Give the extent of all Trypanosoma brucei.
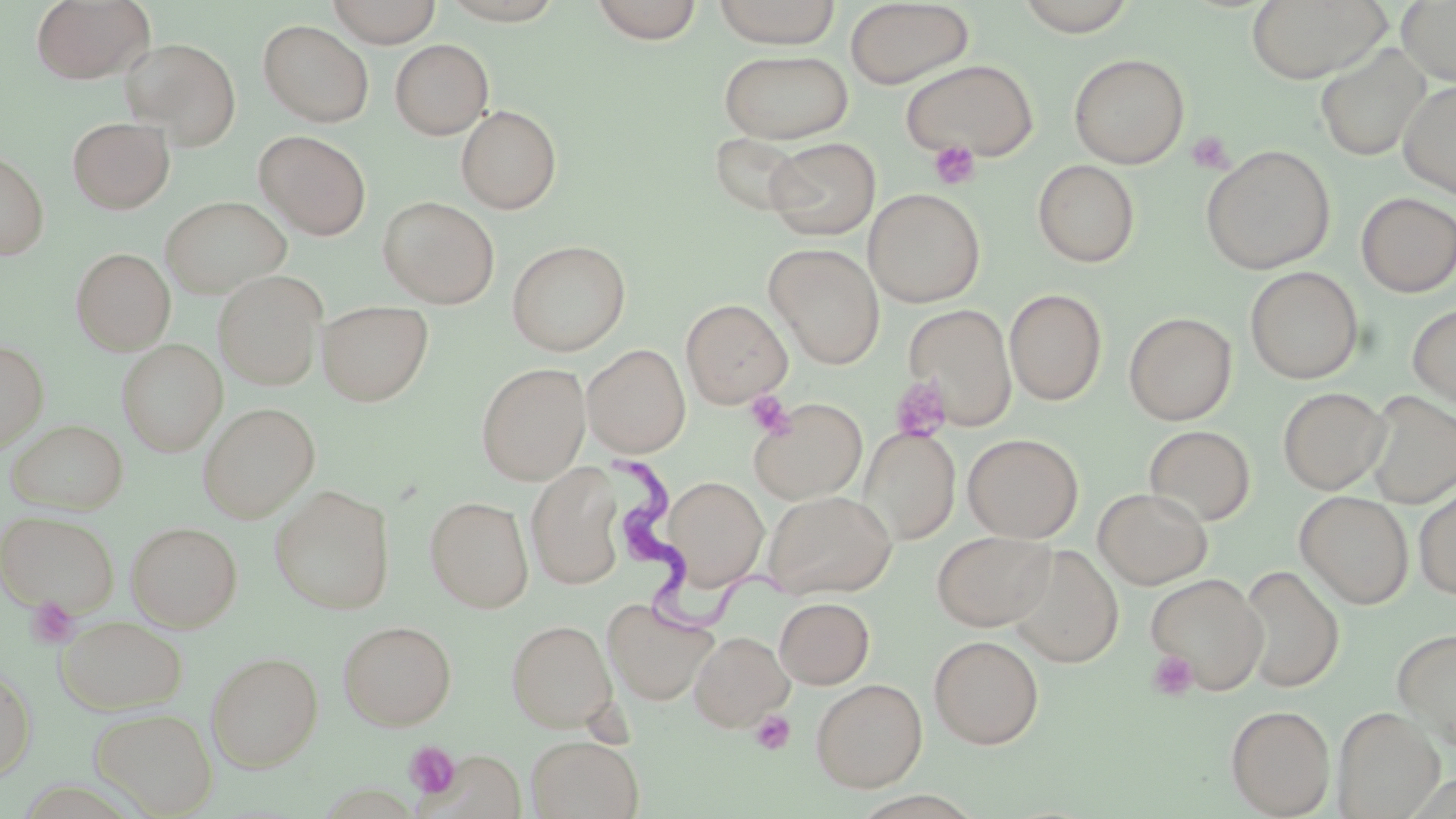

Approximate bounding boxes as [x1, y1, x2, y2] in pixels.
Trypanosoma brucei: [614, 454, 787, 636].

slide_level_diagnosis: Trypanosoma brucei
preparation: thin blood film
platelet_locations: 'approximate bounding boxes as [x1, y1, x2, y2] in pixels: [1187, 131, 1234, 174], [928, 140, 981, 189], [889, 375, 952, 442], [744, 390, 795, 439], [26, 596, 80, 649], [1146, 649, 1200, 700], [750, 710, 796, 755], [404, 741, 461, 800]'
image_size: 1456×819 pixels
magnification: 1000x
uninfected_red_blood_cell_locations: 'approximate bounding boxes as [x1, y1, x2, y2] in pixels: [31, 0, 153, 84], [328, 0, 441, 47], [589, 0, 704, 44], [1013, 0, 1139, 35], [1246, 0, 1392, 84], [1397, 0, 1456, 87], [437, 1, 566, 26], [712, 1, 841, 48], [845, 1, 974, 89], [258, 20, 374, 127], [120, 37, 241, 149], [389, 39, 494, 139], [1315, 43, 1430, 161], [718, 49, 854, 144], [1069, 53, 1189, 168], [901, 59, 1039, 162], [1398, 80, 1456, 197], [456, 105, 562, 214], [67, 117, 175, 214], [256, 130, 371, 240], [710, 131, 810, 218], [765, 137, 880, 239], [1201, 144, 1336, 274], [0, 149, 49, 260], [1033, 160, 1140, 267], [864, 188, 985, 307], [1357, 193, 1456, 297], [161, 196, 292, 298], [378, 196, 500, 308], [506, 240, 630, 356], [764, 243, 885, 369], [71, 248, 174, 355], [1245, 266, 1363, 384], [214, 270, 328, 389], [1005, 289, 1107, 405], [681, 299, 792, 408], [317, 300, 434, 406], [1408, 302, 1456, 409], [903, 303, 1017, 431], [1124, 311, 1237, 425], [0, 340, 48, 453], [117, 340, 226, 455], [582, 344, 690, 457], [476, 362, 591, 485], [1278, 386, 1390, 494], [1362, 390, 1456, 508], [749, 397, 867, 504], [197, 402, 319, 522], [6, 419, 128, 514], [1143, 424, 1256, 526], [859, 427, 961, 545], [962, 433, 1084, 543], [526, 463, 625, 590], [660, 475, 768, 591], [1414, 482, 1456, 600], [269, 485, 395, 614], [1093, 487, 1212, 589], [763, 489, 897, 599], [1294, 491, 1414, 609], [425, 496, 534, 613], [0, 511, 120, 616], [126, 521, 243, 632], [931, 530, 1055, 631], [1007, 545, 1123, 667], [1239, 564, 1344, 692], [1146, 573, 1269, 693], [602, 597, 719, 706], [775, 597, 874, 688], [56, 615, 188, 714], [506, 619, 618, 733], [337, 620, 457, 730], [1393, 626, 1456, 750], [690, 631, 793, 731], [929, 635, 1044, 749], [207, 651, 323, 772], [0, 666, 35, 782], [811, 678, 928, 792], [1226, 704, 1335, 817], [89, 706, 218, 817], [1333, 706, 1444, 818], [526, 735, 644, 819]'
field_of_view: single
modality: light microscopy
stain: May-Grünwald-Giemsa